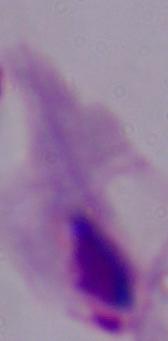

magnification = 1000x
identification = trichomonad
modality = photomicrograph